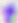
Summary:
  - Modality: micrograph
  - Magnification: 400x
  - Identification: Toxoplasma gondii